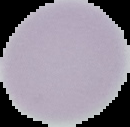
image type = segmented cell region on a black background
preparation = thin blood film
image size = 130×127 pixels
result = no Plasmodium parasites detected